State which parasite is depicted.
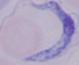

A trypanosome.

Micrograph. Captured at 1000x magnification.